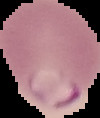

Summary:
  - Malaria status: parasitized
  - Image size: 100×118 pixels
  - Preparation: thin blood film
  - Image type: segmented cell region with the area outside set to black